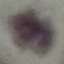

malaria status = uninfected
capture = smartphone through the microscope eyepiece
image type = cell patch, automatically extracted from a larger field of view and resized to 64 × 64 pixels
preparation = thin smear
stain = Giemsa